Give the extent of all Plasmodium parasites.
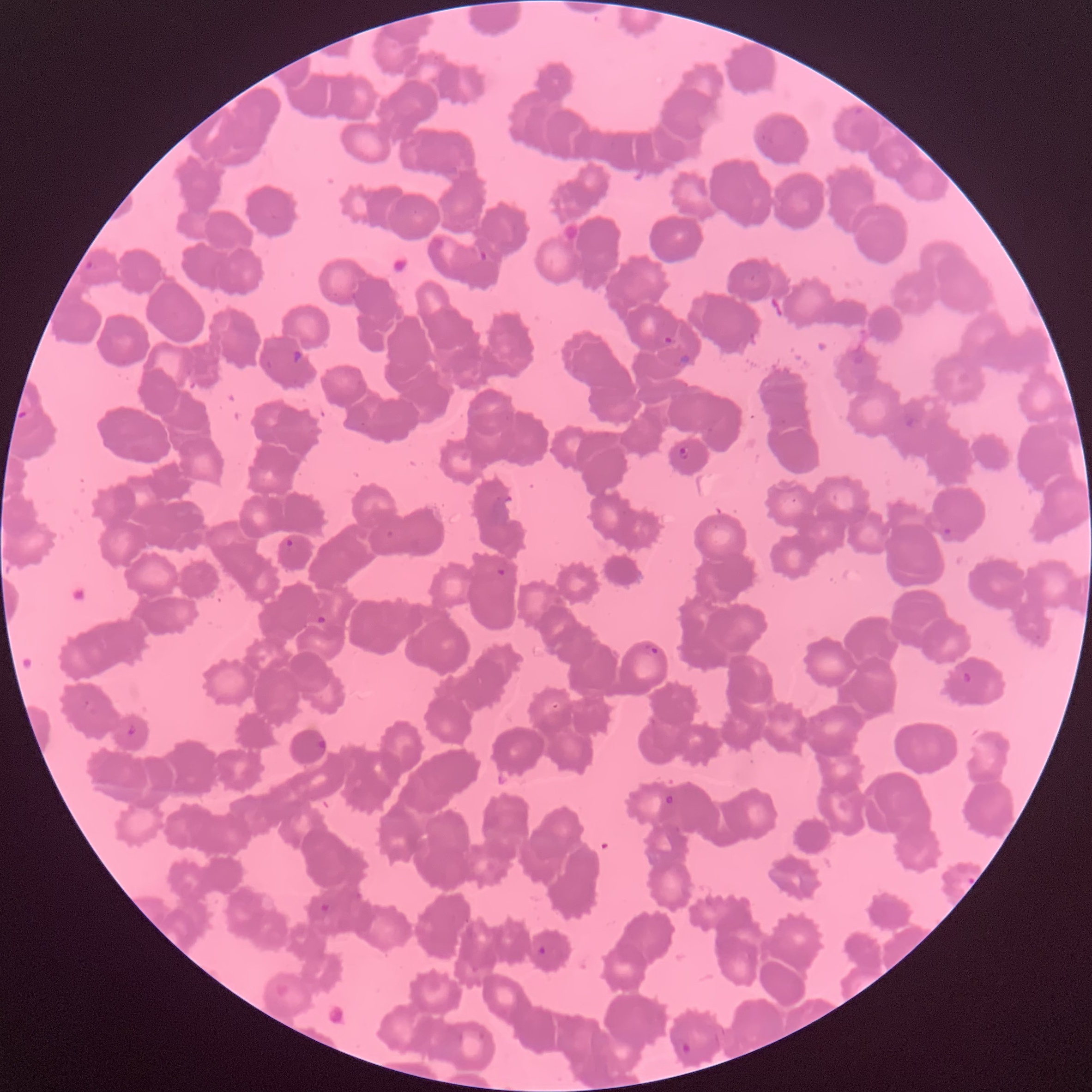
Approximate bounding boxes as [x1, y1, x2, y2] in pixels.
Plasmodium parasites: [477, 249, 488, 264], [662, 334, 674, 346], [291, 349, 303, 365], [678, 352, 690, 365], [902, 414, 917, 429], [678, 446, 690, 460], [943, 527, 952, 535], [385, 530, 395, 540], [284, 538, 295, 549], [496, 567, 506, 578], [315, 614, 328, 626], [645, 643, 659, 657], [960, 670, 973, 686], [125, 725, 138, 738], [318, 737, 327, 752], [664, 794, 675, 806], [319, 902, 330, 914], [537, 945, 547, 955], [681, 1041, 693, 1056].

modality = optical microscopy
preparation = thin blood film
image size = 1092×1092 pixels
red blood cell morphology = rouleaux formation